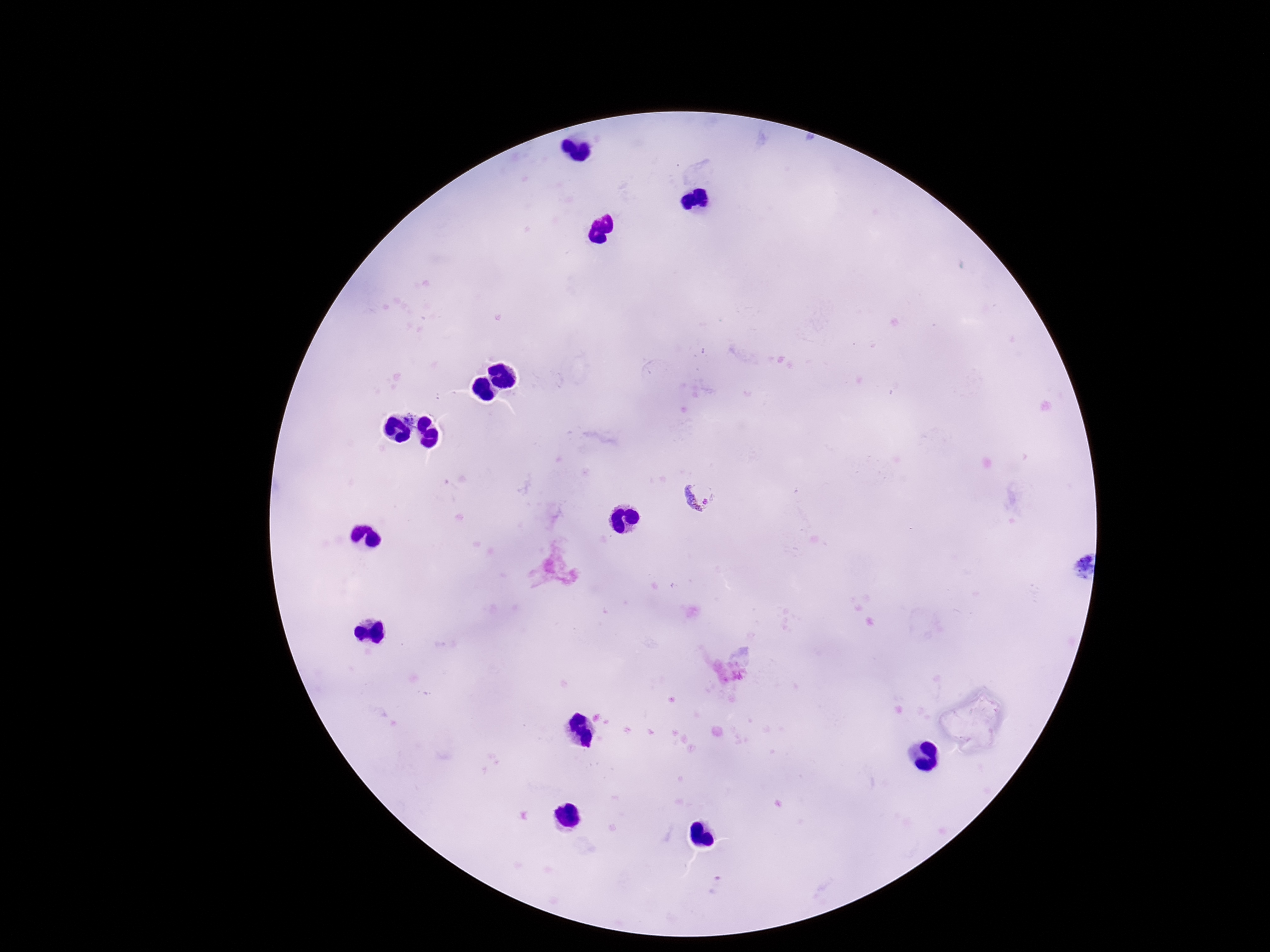
magnification = 100x
stain = Giemsa
field of view = single
image size = 1270×952 pixels
patient malaria status = infected
preparation = thick peripheral-blood smear
capture = smartphone camera through the microscope eyepiece
Plasmodium parasite locations = approximate centers as [x, y] in pixels: [702, 494]